Name the cell type shown.
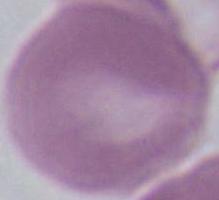
An erythrocyte.

modality = micrograph
magnification = 1000x